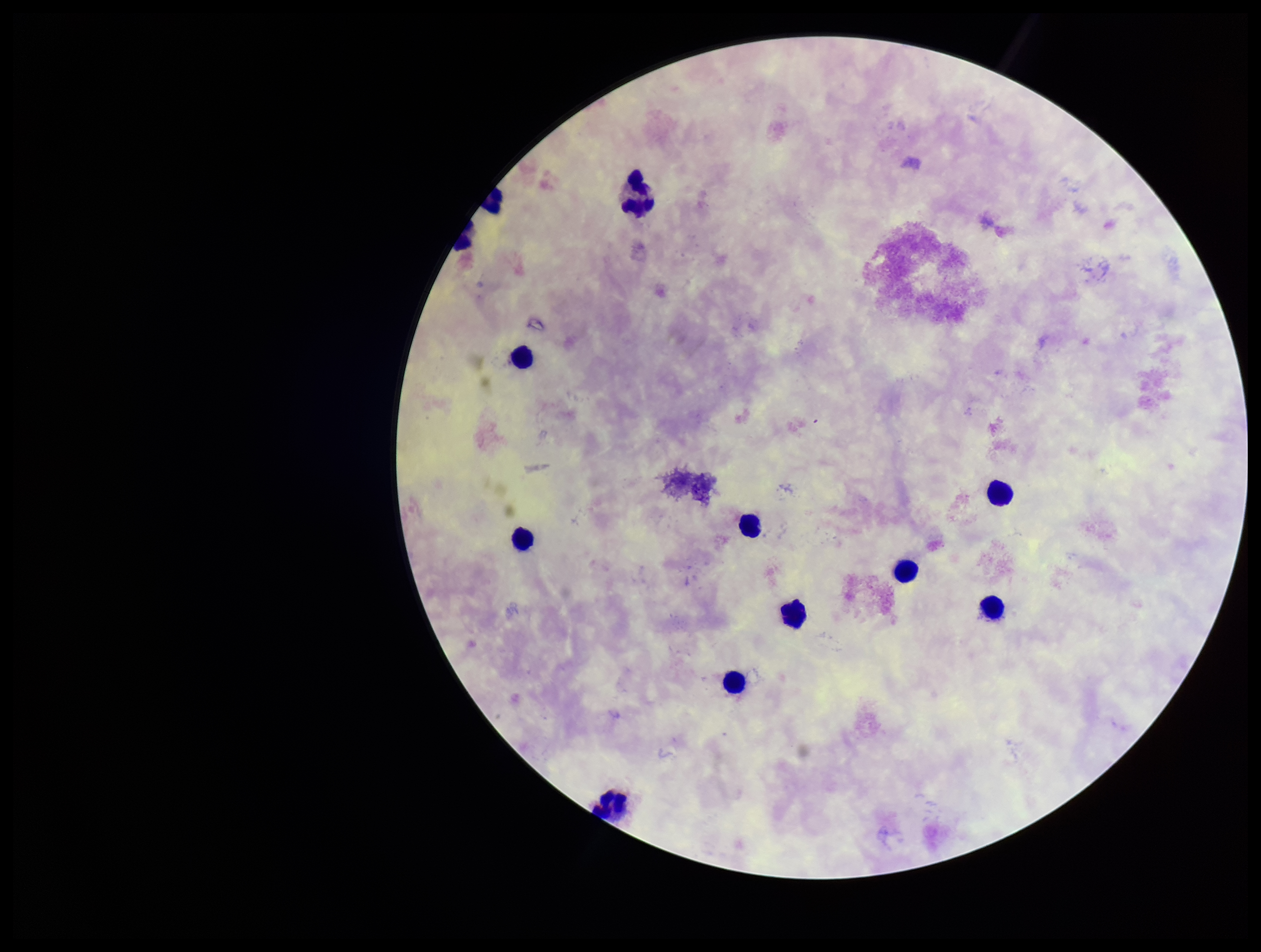

One field from this slide. Image is 1261×952 pixels. Plasmodium parasites: none detected. Patient malaria status: negative. Leukocyte count: 12. Preparation: thick smear. Parasite count: 0. Smartphone photograph taken through the eyepiece of a microscope. Stained with Giemsa.